State the blood parasite species.
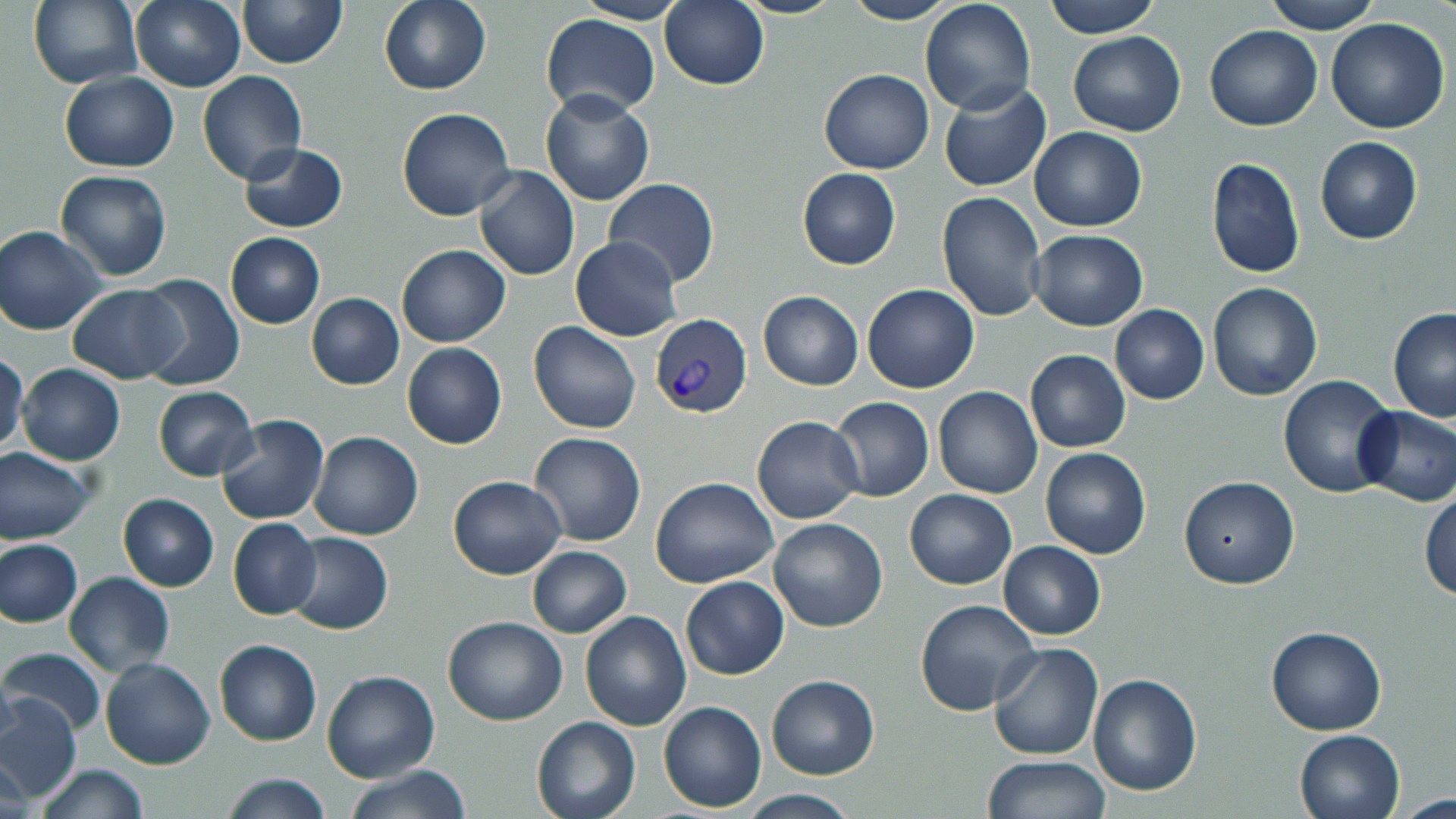
Plasmodium vivax.

Approximate bounding boxes as (x1, y1, x2, y2) in pixels. Plasmodium vivax-infected red blood cell locations: (650, 314, 753, 419). Uninfected red blood cell locations: (28, 0, 142, 90), (130, 0, 247, 91), (237, 0, 345, 68), (576, 0, 690, 24), (660, 0, 768, 91), (1043, 0, 1161, 38), (1262, 0, 1380, 34), (379, 1, 492, 94), (841, 1, 960, 25), (919, 1, 1036, 116), (541, 12, 660, 121), (1326, 19, 1450, 134), (1205, 25, 1322, 130), (1067, 31, 1187, 136), (820, 68, 934, 175), (198, 71, 306, 185), (59, 72, 180, 172), (939, 83, 1050, 192), (540, 91, 654, 206), (397, 107, 517, 221), (1028, 127, 1146, 232), (1315, 137, 1423, 245), (239, 142, 348, 233), (1206, 157, 1305, 280), (474, 167, 580, 282), (797, 168, 901, 270), (55, 170, 172, 281), (603, 178, 720, 288), (937, 192, 1046, 321), (1, 224, 106, 334), (1028, 229, 1149, 330), (225, 233, 325, 329), (570, 237, 683, 341), (396, 245, 509, 347), (135, 274, 244, 390), (1208, 282, 1323, 402), (67, 284, 186, 383), (863, 284, 979, 394), (758, 291, 863, 390), (306, 293, 404, 390), (1111, 304, 1209, 404), (1388, 308, 1456, 422), (530, 321, 641, 434), (402, 342, 507, 449), (0, 350, 28, 457), (1025, 350, 1130, 453), (17, 363, 125, 465), (1278, 375, 1395, 497), (152, 386, 258, 482), (934, 386, 1042, 498), (829, 396, 934, 502), (1352, 405, 1456, 506), (215, 413, 330, 525), (752, 416, 864, 523), (310, 430, 423, 541), (529, 430, 647, 547), (1, 446, 96, 544), (1040, 448, 1150, 559), (446, 475, 567, 579), (1179, 475, 1299, 589), (649, 477, 779, 588), (904, 489, 1016, 589), (1420, 489, 1455, 598), (118, 493, 219, 590), (227, 518, 322, 621), (768, 518, 889, 633), (285, 532, 393, 634), (0, 537, 84, 628), (998, 540, 1106, 639), (527, 546, 632, 638), (64, 572, 174, 676), (680, 575, 789, 680), (915, 600, 1041, 718), (579, 610, 692, 730), (442, 614, 568, 725), (1265, 624, 1387, 734), (215, 639, 321, 747), (988, 643, 1105, 761), (0, 647, 106, 738), (100, 657, 216, 770), (322, 671, 440, 784), (1087, 674, 1201, 795), (766, 675, 880, 780), (0, 692, 82, 803), (658, 700, 766, 813), (532, 716, 641, 819), (1294, 729, 1405, 819), (982, 754, 1112, 818), (35, 763, 148, 819), (343, 764, 471, 819), (221, 774, 331, 818), (738, 789, 863, 818). Optical microscopy. Captured at 1000x magnification. Thin blood film. May-Grünwald-Giemsa-stained preparation. Image is 1456×819 pixels. One field of a larger specimen.